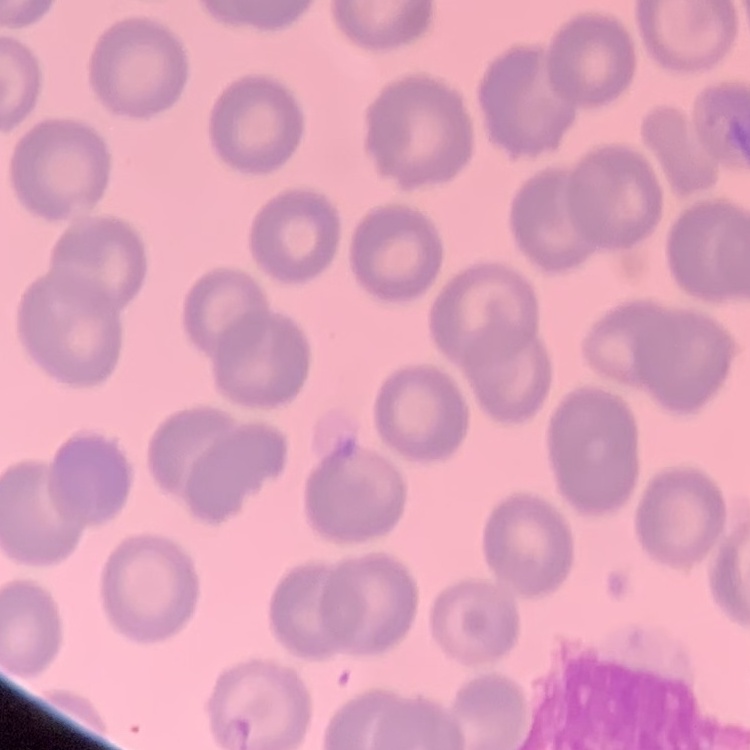

erythrocyte morphology = no rouleaux formation
image type = one tile cut from a larger photomicrograph
preparation = thin blood film
stain = Field's or Giemsa